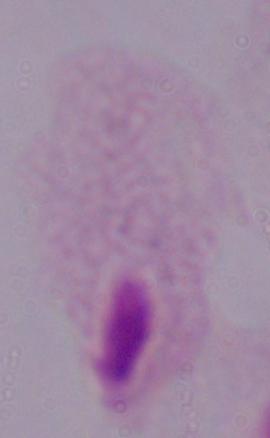 A trichomonad is seen. Micrograph. 1000x magnification.